Locate every malaria parasite.
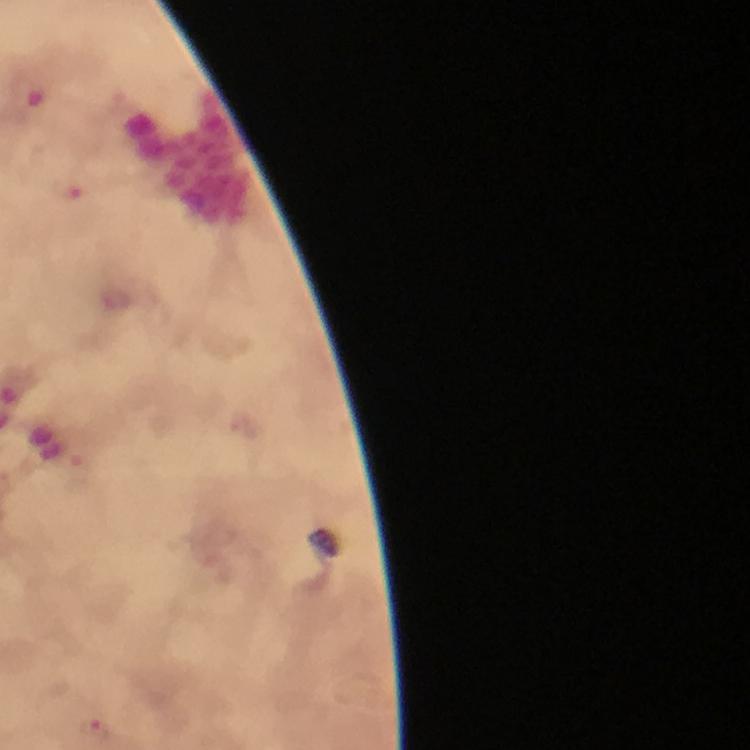
Approximate object centers, in pixels from the top-left corner.
Malaria parasites: (x=69, y=192), (x=95, y=730).

Summary:
  - Magnification: 100x
  - Preparation: thick blood film
  - Context: from a malaria diagnostic workup
  - Cropped from: a single field of view
  - Image size: 750×750 pixels
  - Stain: Giemsa
  - Capture: smartphone photograph through a microscope
  - Immersion oil: applied